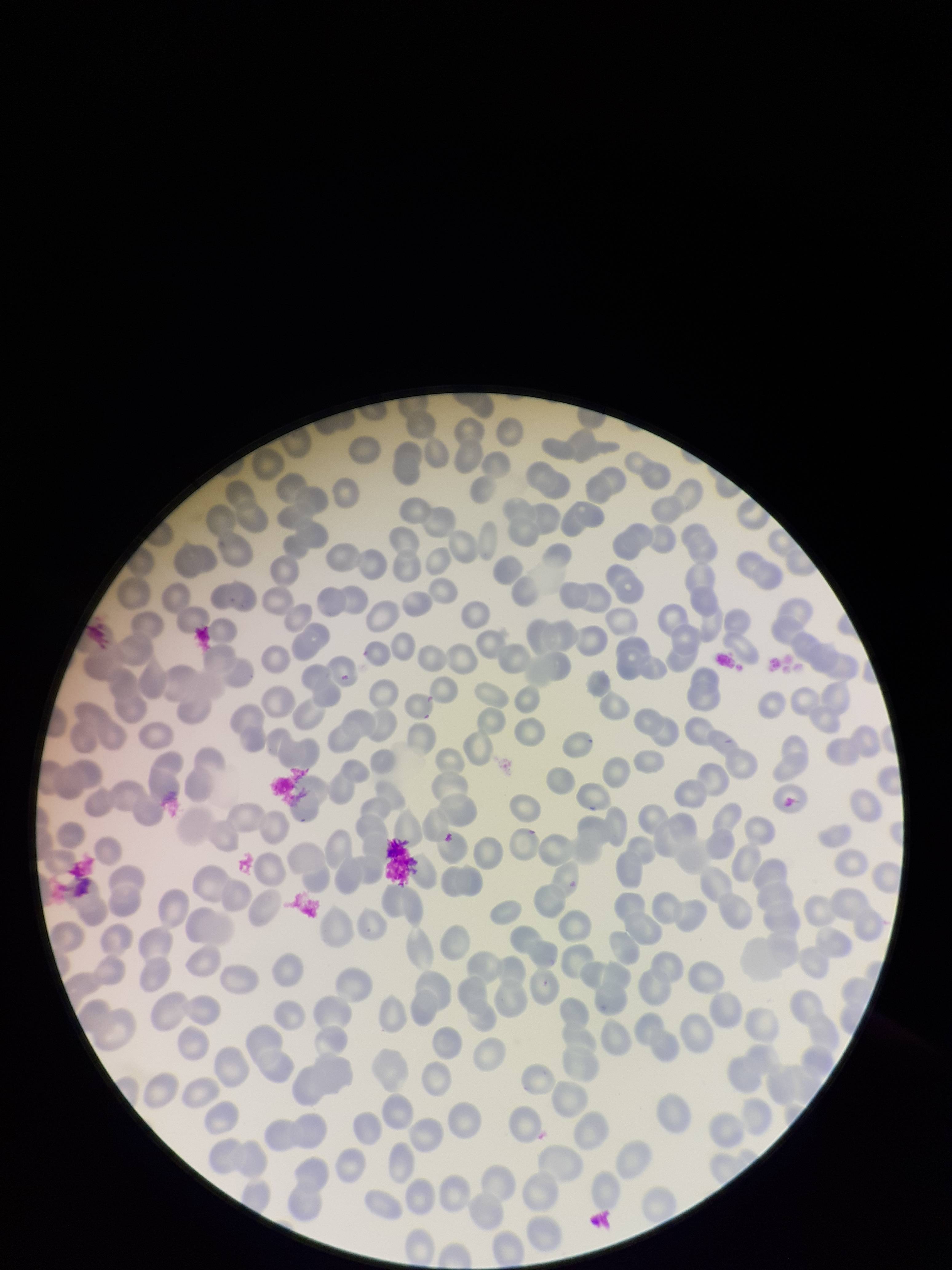
Summary:
  - Image size: 952×1270 pixels
  - Stain: Giemsa
  - Parasitized red blood cells: none identified
  - Field of view: one from this slide
  - Capture: smartphone photograph through the microscope eyepiece
  - Red blood cell count: 239
  - Preparation: thin blood smear
  - Patient malaria status: negative
  - Parasitized red blood cell count: 0